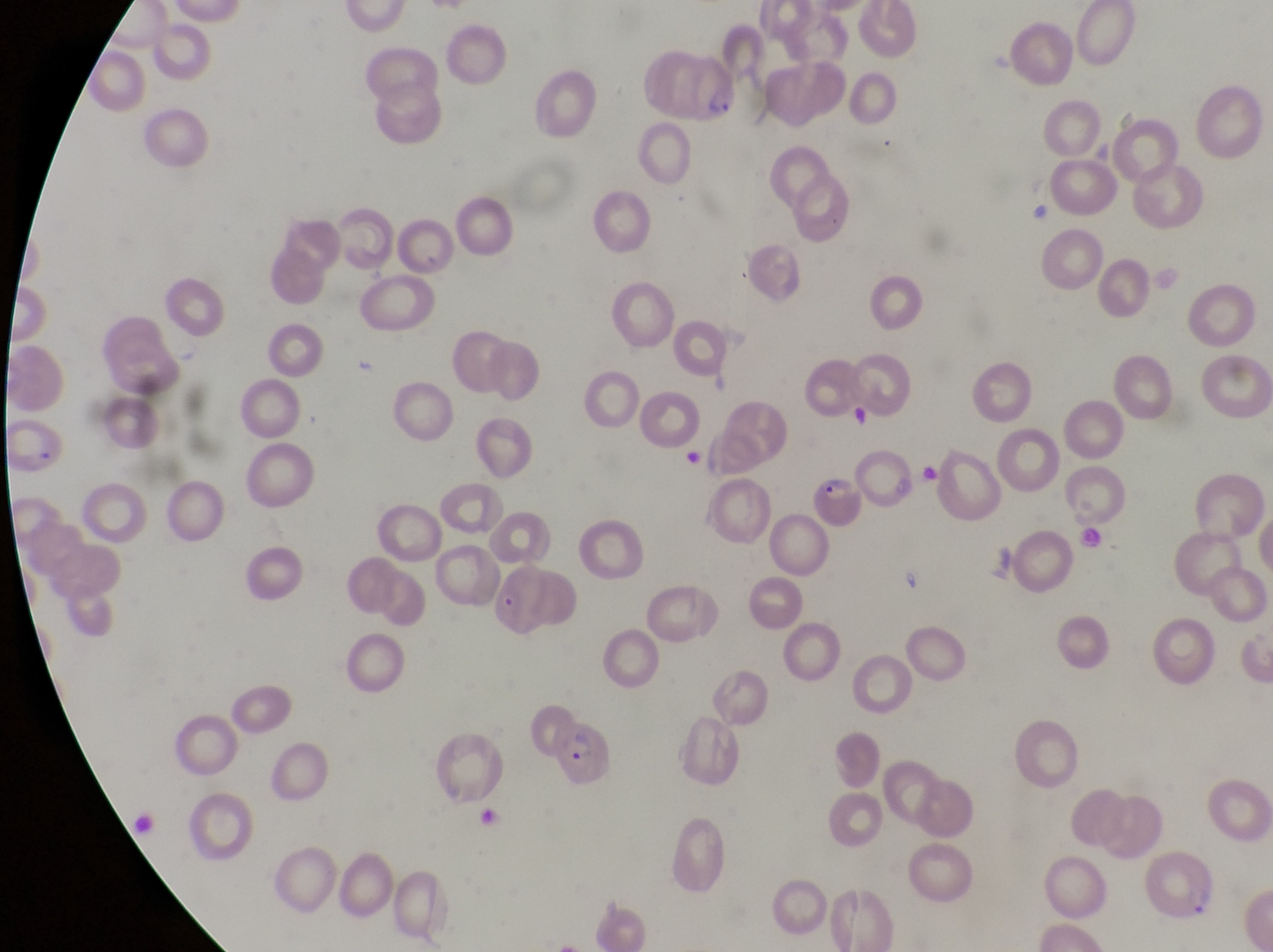
magnification = 1000x
capture = smartphone photograph through the eyepiece of an Olympus CX-23 microscope
country = Uganda
field of view = single
preparation = thin blood smear
parasitised red blood cell locations = approximate bounding boxes as [left, top, right, bottom] in pixels: [643, 52, 741, 127], [811, 474, 864, 534], [501, 564, 585, 640], [549, 721, 616, 786]
image size = 1273×952 pixels